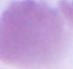
Summary:
  - Magnification: 1000x
  - Identification: red blood cell
  - Modality: photomicrograph